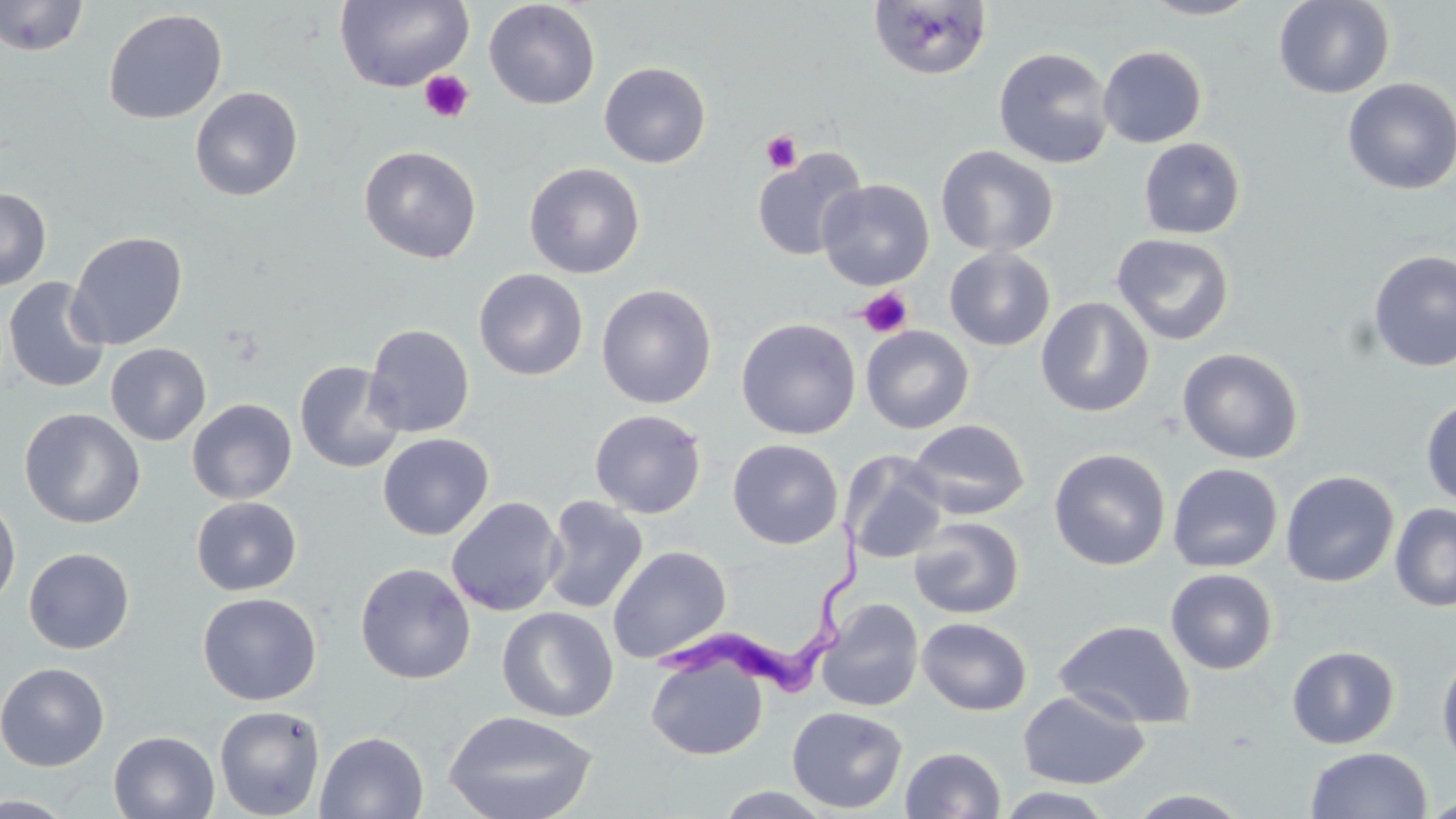

Summary:
  - Coordinate format: approximate bounding boxes as (x1, y1, x2, y2) in pixels
  - Uninfected red blood cell locations: (0, 0, 90, 57), (1138, 0, 1265, 20), (1273, 0, 1395, 99), (333, 1, 474, 92), (483, 1, 601, 110), (867, 1, 992, 80), (103, 8, 227, 124), (1097, 45, 1207, 148), (993, 46, 1115, 169), (598, 61, 712, 168), (1341, 77, 1456, 195), (190, 86, 303, 201), (1138, 137, 1246, 239), (358, 145, 482, 264), (935, 145, 1059, 257), (751, 147, 867, 262), (524, 162, 645, 279), (816, 178, 935, 290), (0, 187, 51, 291), (66, 231, 188, 351), (1111, 232, 1236, 346), (944, 246, 1056, 351), (1368, 250, 1456, 373), (473, 268, 589, 381), (2, 276, 111, 393), (596, 283, 717, 409), (1036, 296, 1155, 417), (736, 317, 861, 440), (363, 323, 475, 438), (860, 326, 974, 434), (105, 343, 211, 446), (1177, 347, 1304, 464), (294, 360, 405, 473), (1420, 396, 1456, 509), (186, 398, 297, 504), (19, 408, 145, 528), (589, 409, 707, 519), (907, 418, 1030, 520), (377, 433, 494, 540), (727, 439, 844, 549), (1049, 447, 1171, 571), (841, 451, 948, 565), (1167, 462, 1283, 573), (1280, 470, 1399, 588), (0, 493, 21, 611), (541, 495, 649, 615), (191, 496, 302, 596), (446, 496, 565, 617), (1390, 504, 1456, 612), (908, 516, 1025, 619), (607, 545, 732, 664), (23, 547, 135, 654), (354, 562, 476, 684), (1165, 568, 1279, 675), (197, 591, 321, 705), (816, 598, 924, 712), (497, 607, 618, 723), (917, 617, 1032, 715), (1054, 619, 1195, 729), (1286, 645, 1399, 749), (1436, 648, 1456, 773), (646, 656, 768, 760), (0, 661, 110, 771), (1017, 689, 1150, 789), (214, 705, 325, 819), (786, 705, 908, 814), (443, 710, 599, 819), (108, 729, 220, 819), (315, 731, 429, 818), (900, 746, 1006, 819), (1305, 746, 1432, 819), (708, 785, 839, 818), (994, 787, 1117, 819), (1124, 789, 1255, 818), (0, 794, 80, 819), (1420, 794, 1456, 817)
  - Platelet locations: (419, 70, 474, 123), (761, 130, 803, 173), (857, 287, 913, 338)
  - Trypanosoma brucei locations: (656, 521, 871, 698)
  - Slide-level diagnosis: Trypanosoma brucei
  - Magnification: 1000x
  - Modality: optical microscopy
  - Field of view: one of a larger specimen
  - Image size: 1456×819 pixels
  - Stain: May-Grünwald-Giemsa
  - Preparation: thin blood film